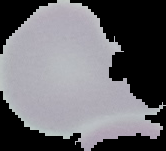

{
  "image_size": "166×151 pixels",
  "result": "no malaria parasites detected",
  "preparation": "thin blood smear",
  "image_type": "segmented cell region with the area outside set to black"
}